Outline each blood parasite and name the species.
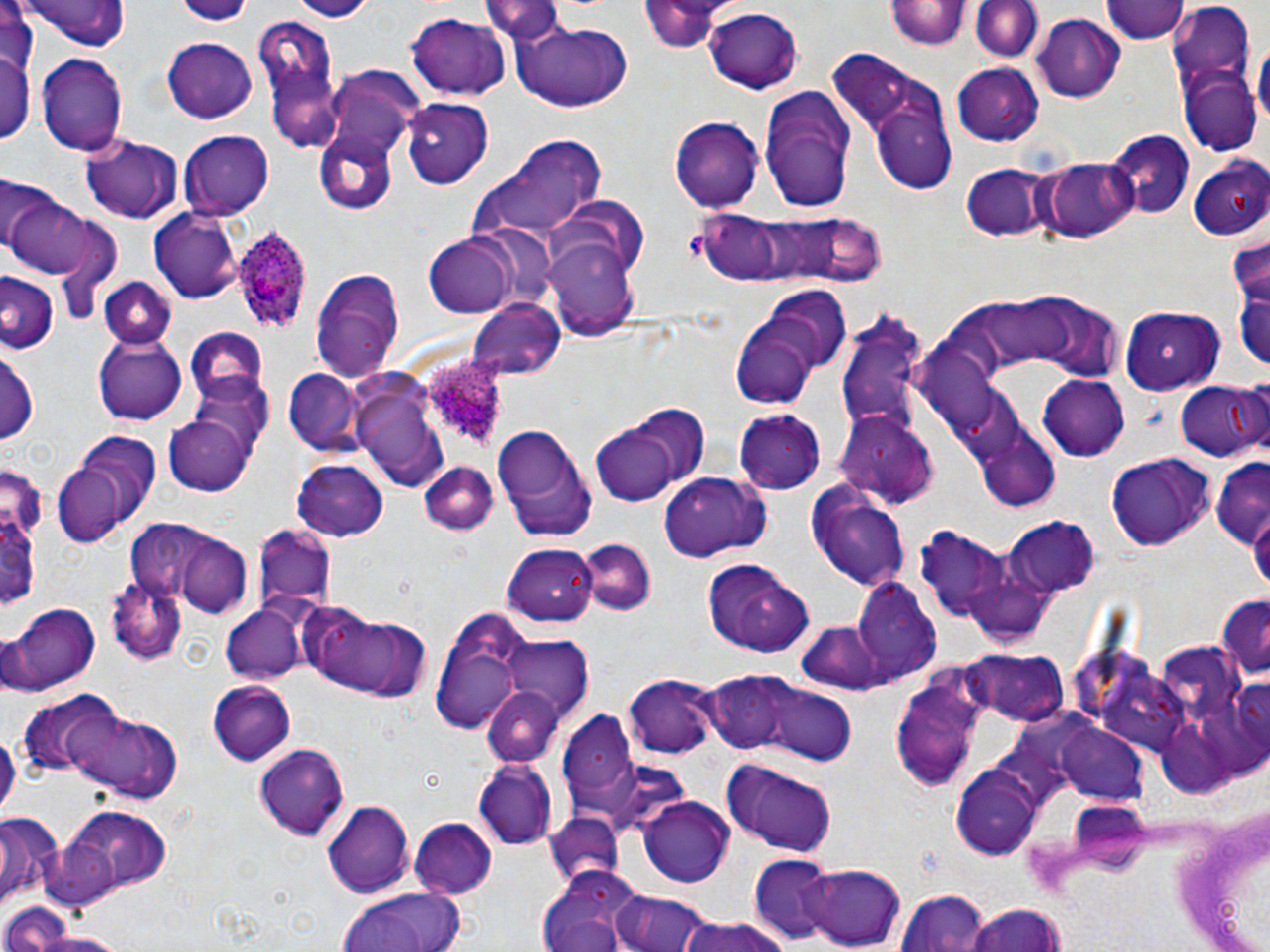

Approximate bounding boxes as (x1, y1, x2, y2) in pixels.
Plasmodium ovale-infected red blood cells: (227, 225, 317, 337), (421, 353, 516, 452).
No Plasmodium falciparum, Plasmodium malariae, Plasmodium vivax, Babesia divergens, or Trypanosoma brucei observed.

slide-level diagnosis = Plasmodium ovale
magnification = 1000x
field of view = single
preparation = thin blood smear
modality = optical microscopy
stain = May-Grünwald-Giemsa
platelet locations = approximate bounding boxes as (x1, y1, x2, y2) in pixels: (680, 226, 707, 262)
uninfected red blood cell locations = approximate bounding boxes as (x1, y1, x2, y2) in pixels: (18, 0, 131, 51), (172, 0, 255, 25), (283, 0, 376, 21), (483, 0, 564, 43), (641, 0, 729, 51), (968, 0, 1045, 62), (1100, 0, 1186, 44), (886, 1, 968, 51), (1167, 4, 1257, 161), (704, 8, 804, 95), (404, 11, 511, 101), (1034, 14, 1124, 102), (510, 19, 633, 113), (255, 20, 346, 145), (1255, 37, 1268, 140), (162, 39, 257, 123), (1, 44, 34, 144), (36, 52, 128, 156), (832, 55, 954, 190), (950, 64, 1045, 145), (325, 66, 429, 154), (757, 84, 855, 211), (870, 99, 958, 194), (402, 100, 496, 189), (670, 117, 764, 211), (180, 129, 275, 216), (1108, 129, 1194, 219), (314, 132, 399, 214), (81, 135, 183, 222), (484, 135, 607, 235), (1186, 154, 1270, 241), (1043, 159, 1136, 242), (961, 162, 1052, 242), (0, 177, 54, 257), (6, 191, 103, 280), (544, 200, 647, 290), (148, 208, 243, 303), (690, 211, 883, 293), (1229, 231, 1269, 309), (422, 233, 521, 318), (542, 241, 641, 342), (310, 268, 406, 384), (0, 275, 57, 354), (98, 279, 176, 350), (1232, 280, 1270, 376), (761, 284, 853, 371), (1035, 291, 1124, 375), (977, 295, 1075, 365), (468, 298, 566, 380), (1118, 305, 1228, 397), (835, 311, 933, 440), (731, 319, 817, 410), (184, 328, 270, 407), (93, 336, 187, 424), (898, 340, 1001, 432), (1, 347, 39, 446), (283, 369, 367, 456), (186, 374, 275, 469), (1039, 375, 1131, 460), (355, 376, 453, 493), (1173, 377, 1268, 461), (945, 384, 1027, 468), (616, 404, 709, 492), (736, 410, 829, 492), (837, 410, 941, 507), (165, 416, 255, 496), (492, 423, 597, 540), (593, 425, 681, 506), (982, 443, 1060, 513), (50, 447, 143, 547), (1107, 454, 1212, 551), (1212, 457, 1270, 547), (294, 458, 389, 540), (417, 464, 497, 535), (0, 472, 41, 621), (659, 473, 768, 561), (803, 482, 910, 593), (1007, 518, 1102, 599), (146, 523, 255, 618), (254, 525, 335, 608), (915, 530, 1013, 624), (578, 540, 654, 616), (502, 545, 596, 625), (702, 559, 813, 659), (108, 577, 189, 663), (853, 580, 943, 684), (1215, 594, 1269, 683), (8, 603, 99, 695), (220, 606, 306, 683), (300, 606, 431, 701), (429, 608, 533, 733), (795, 622, 884, 694), (501, 637, 595, 723), (1158, 640, 1249, 718), (1063, 642, 1151, 721), (961, 649, 1069, 727), (1098, 665, 1185, 756), (697, 672, 829, 761), (890, 674, 986, 791), (622, 676, 724, 761), (208, 681, 296, 764), (482, 686, 565, 765), (767, 688, 857, 766), (21, 695, 118, 779), (56, 702, 181, 804), (556, 712, 639, 802), (1055, 721, 1151, 804), (1155, 722, 1238, 801), (253, 744, 350, 840), (472, 761, 558, 850), (723, 761, 840, 857), (950, 770, 1041, 857), (638, 796, 734, 887), (322, 799, 414, 897), (1170, 803, 1270, 952), (45, 804, 173, 902), (545, 813, 623, 886), (0, 815, 60, 903), (409, 819, 495, 899), (748, 856, 845, 945), (800, 864, 907, 949), (539, 865, 649, 950), (335, 886, 472, 952), (611, 888, 717, 952), (894, 890, 991, 952), (963, 903, 1066, 952), (3, 905, 117, 952), (678, 915, 797, 952), (19, 927, 132, 952)
image size = 1270×952 pixels